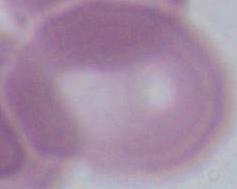

identification: erythrocyte
modality: photomicrograph
magnification: 1000x